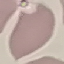
{
  "malaria_status": "uninfected",
  "image_type": "cell patch, automatically extracted from a larger field of view and resized to 64 × 64 pixels",
  "preparation": "thin blood film",
  "stain": "Giemsa",
  "capture": "smartphone camera at the microscope eyepiece"
}